Assess this cell for malaria.
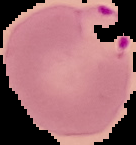
It is parasitized.

{
  "image_size": "136×145 pixels",
  "image_type": "segmented cell region on a black background",
  "preparation": "thin blood smear"
}